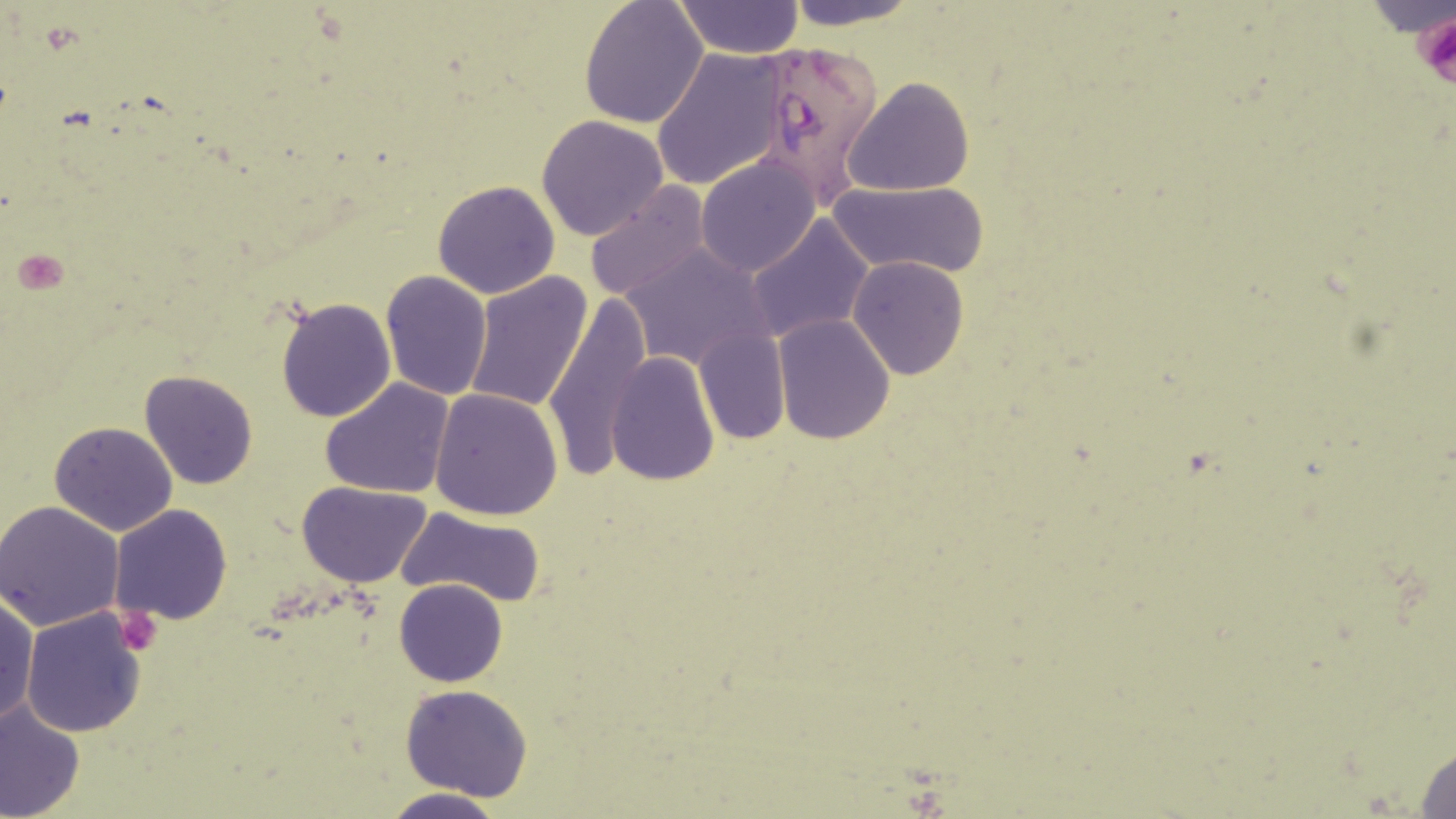

slide-level diagnosis = Plasmodium falciparum
preparation = thin blood smear
image size = 1456×819 pixels
modality = optical microscopy
field of view = single
uninfected red blood cell locations = approximate bounding boxes as named x1/y1/x2/y2 corners in pixels: (x1=578, y1=0, x2=708, y2=128), (x1=781, y1=0, x2=922, y2=29), (x1=673, y1=2, x2=804, y2=59), (x1=650, y1=48, x2=790, y2=191), (x1=842, y1=77, x2=975, y2=197), (x1=537, y1=115, x2=671, y2=242), (x1=695, y1=156, x2=820, y2=277), (x1=432, y1=179, x2=561, y2=298), (x1=828, y1=180, x2=989, y2=276), (x1=584, y1=183, x2=712, y2=304), (x1=746, y1=215, x2=873, y2=343), (x1=620, y1=243, x2=771, y2=372), (x1=847, y1=257, x2=969, y2=381), (x1=380, y1=269, x2=493, y2=401), (x1=464, y1=272, x2=593, y2=414), (x1=275, y1=297, x2=396, y2=422), (x1=544, y1=300, x2=652, y2=479), (x1=772, y1=312, x2=895, y2=445), (x1=693, y1=327, x2=790, y2=445), (x1=605, y1=352, x2=719, y2=486), (x1=140, y1=369, x2=259, y2=489), (x1=319, y1=378, x2=457, y2=498), (x1=430, y1=387, x2=563, y2=520), (x1=65, y1=392, x2=250, y2=515), (x1=50, y1=422, x2=178, y2=536), (x1=295, y1=479, x2=433, y2=586), (x1=0, y1=501, x2=124, y2=632), (x1=110, y1=504, x2=233, y2=626), (x1=395, y1=506, x2=547, y2=608), (x1=395, y1=578, x2=507, y2=687), (x1=0, y1=592, x2=37, y2=727), (x1=19, y1=607, x2=147, y2=736), (x1=400, y1=684, x2=534, y2=802), (x1=0, y1=703, x2=84, y2=818), (x1=1412, y1=743, x2=1456, y2=818), (x1=379, y1=789, x2=508, y2=819)
Plasmodium falciparum-infected red blood cell locations = approximate bounding boxes as named x1/y1/x2/y2 corners in pixels: (x1=751, y1=35, x2=887, y2=208)
stain = May-Grünwald-Giemsa
platelet locations = approximate bounding boxes as named x1/y1/x2/y2 corners in pixels: (x1=1412, y1=12, x2=1456, y2=96), (x1=13, y1=249, x2=69, y2=293), (x1=110, y1=602, x2=166, y2=658)
magnification = 1000x